Locate and identify every blood parasite.
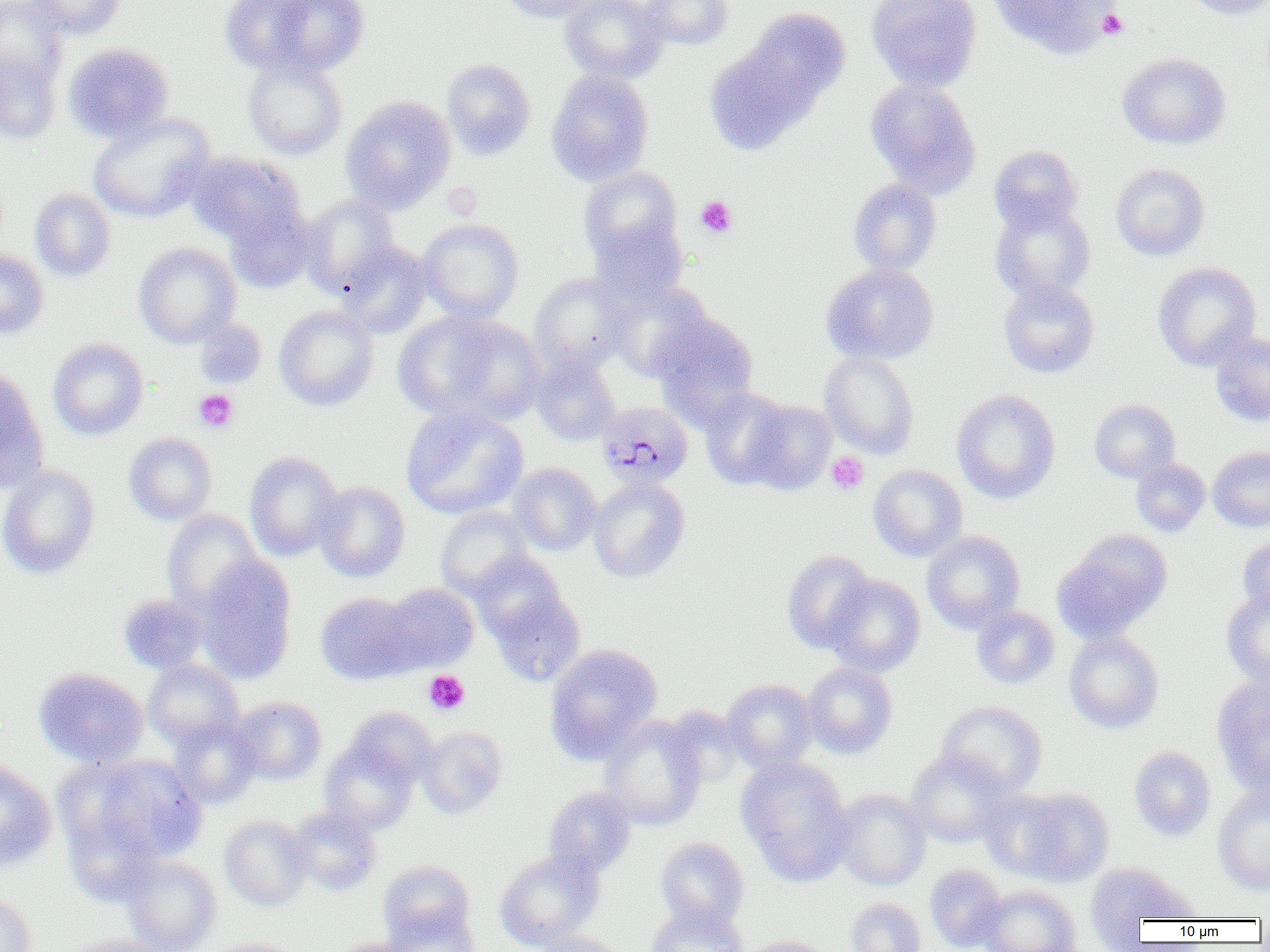

Approximate bounding boxes as (x1, y1, x2, y2) in pixels.
Plasmodium malariae-infected red blood cells: (598, 401, 693, 490).
No Plasmodium falciparum, Plasmodium ovale, Plasmodium vivax, Babesia divergens, or Trypanosoma brucei observed.

Uninfected red blood cell locations: (0, 0, 68, 86), (26, 0, 125, 40), (218, 0, 320, 76), (263, 0, 370, 77), (498, 0, 603, 23), (559, 0, 668, 83), (641, 0, 733, 50), (866, 0, 982, 91), (988, 0, 1116, 57), (1180, 0, 1270, 19), (745, 8, 851, 107), (0, 14, 120, 100), (63, 43, 174, 143), (704, 44, 816, 154), (0, 51, 61, 144), (1115, 52, 1220, 261), (1117, 52, 1230, 149), (243, 57, 347, 160), (442, 58, 536, 160), (546, 69, 654, 186), (865, 78, 981, 197), (341, 96, 456, 213), (87, 113, 215, 222), (989, 145, 1083, 234), (187, 152, 304, 247), (1111, 163, 1209, 260), (578, 166, 683, 263), (848, 178, 941, 275), (30, 188, 116, 282), (300, 194, 399, 295), (989, 200, 1095, 303), (224, 202, 316, 293), (417, 219, 523, 322), (589, 219, 689, 306), (133, 242, 241, 347), (338, 242, 433, 338), (0, 247, 49, 339), (1153, 262, 1261, 371), (821, 263, 938, 364), (530, 272, 631, 371), (998, 279, 1099, 378), (607, 281, 714, 381), (274, 305, 379, 411), (393, 311, 503, 420), (651, 313, 760, 426), (441, 317, 547, 424), (194, 319, 268, 389), (1210, 332, 1270, 426), (48, 337, 148, 440), (820, 351, 919, 458), (530, 353, 620, 445), (0, 366, 49, 494), (699, 387, 795, 489), (951, 389, 1060, 504), (743, 399, 837, 494), (1089, 399, 1180, 483), (400, 405, 528, 519), (123, 432, 217, 525), (1208, 446, 1270, 532), (244, 451, 344, 561), (1131, 458, 1210, 536), (508, 463, 601, 555), (0, 464, 100, 579), (868, 464, 967, 561), (588, 477, 690, 583), (313, 481, 410, 582), (436, 507, 533, 599), (162, 510, 263, 616), (1057, 530, 1172, 640), (922, 531, 1025, 633), (1238, 535, 1270, 618), (781, 550, 876, 653), (469, 552, 568, 642), (195, 555, 297, 683), (823, 573, 926, 676), (383, 583, 479, 672), (488, 588, 585, 686), (1221, 588, 1270, 686), (316, 592, 420, 684), (119, 594, 208, 674), (971, 606, 1059, 688), (1064, 631, 1163, 733), (544, 643, 662, 762), (143, 659, 244, 749), (802, 662, 897, 758), (34, 667, 149, 768), (1211, 676, 1270, 794), (722, 678, 819, 772), (232, 696, 327, 784), (936, 700, 1046, 796), (346, 707, 437, 786), (167, 716, 261, 809), (599, 716, 706, 830), (417, 726, 507, 819), (320, 739, 418, 835), (1129, 746, 1216, 841), (905, 750, 1014, 847), (81, 755, 207, 864), (736, 757, 856, 885), (0, 760, 57, 871), (1212, 785, 1270, 895), (543, 786, 636, 876), (1009, 787, 1114, 887), (833, 789, 930, 891), (980, 789, 1070, 878), (63, 806, 165, 908), (287, 806, 381, 895), (220, 815, 311, 910), (655, 836, 749, 930), (495, 848, 604, 950), (122, 855, 221, 952), (378, 859, 475, 944), (1084, 862, 1197, 943), (925, 864, 1007, 952), (976, 885, 1082, 952), (0, 892, 37, 952), (845, 898, 926, 952), (646, 903, 748, 952), (382, 909, 480, 952), (533, 930, 628, 952), (59, 935, 178, 952), (741, 936, 837, 952), (206, 938, 300, 952), (330, 938, 420, 952). Platelet locations: (1097, 9, 1129, 40), (443, 182, 482, 219), (695, 196, 737, 238), (193, 388, 239, 433), (827, 451, 868, 494), (424, 670, 470, 715). Slide-level diagnosis: Plasmodium malariae. Captured at 1000x magnification. Image is 1270×952 pixels. Optical microscopy. Thin blood smear. One field of a larger specimen.